Name the parasite shown.
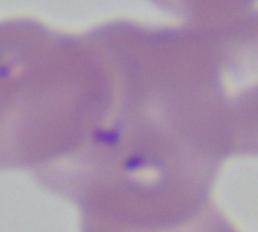

This is Babesia.

Micrograph. Captured at 1000x magnification.